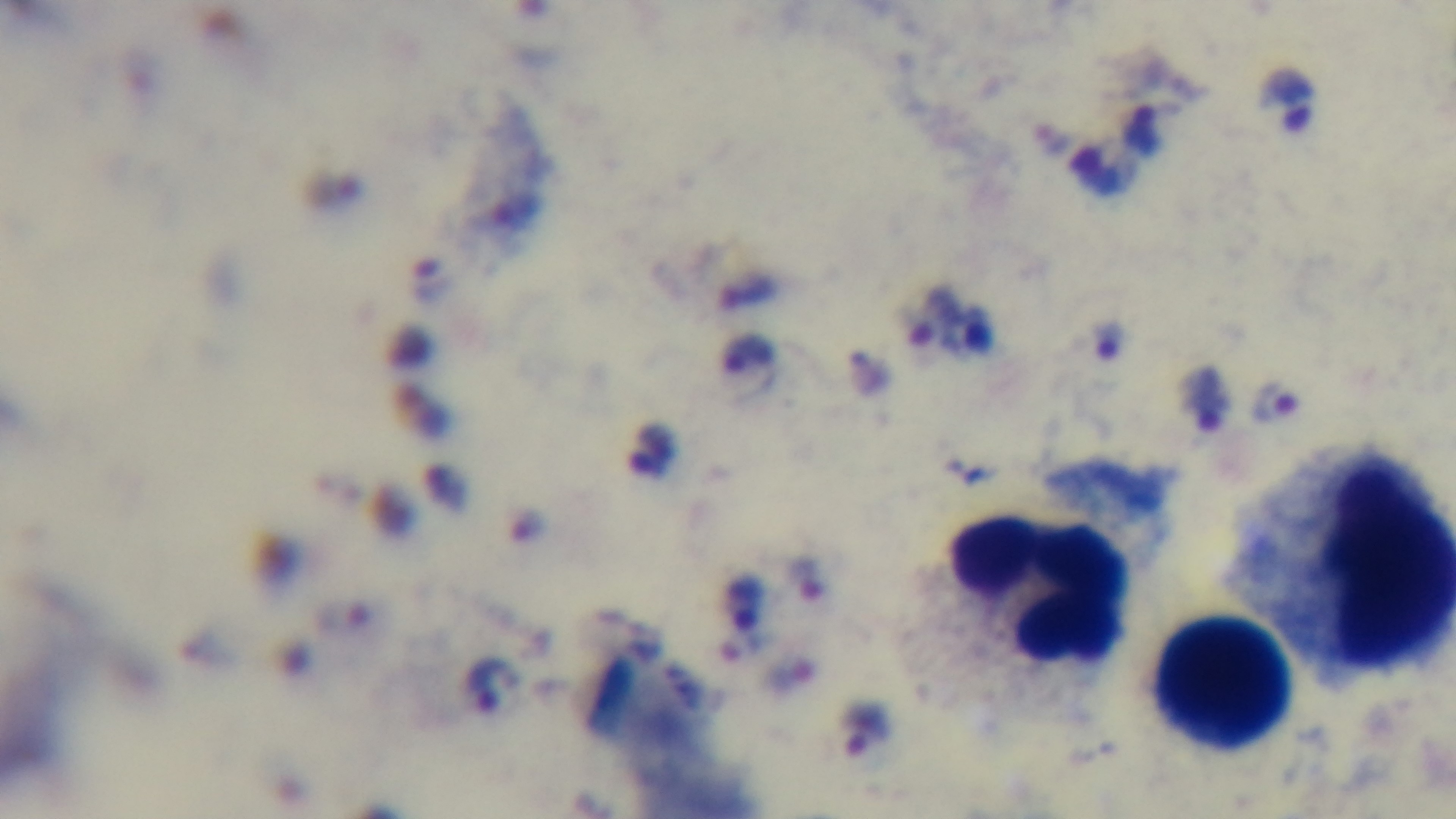

malaria status = positive
objective = 100x oil immersion
preparation = thick smear
capture = mounted 4K digital camera
modality = light microscopy
field of view = single
stain = Giemsa